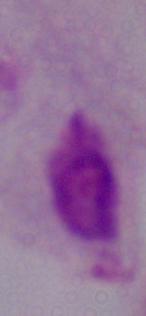

{
  "magnification": "1000x",
  "modality": "micrograph",
  "identification": "trichomonad"
}